Name the blood parasite species.
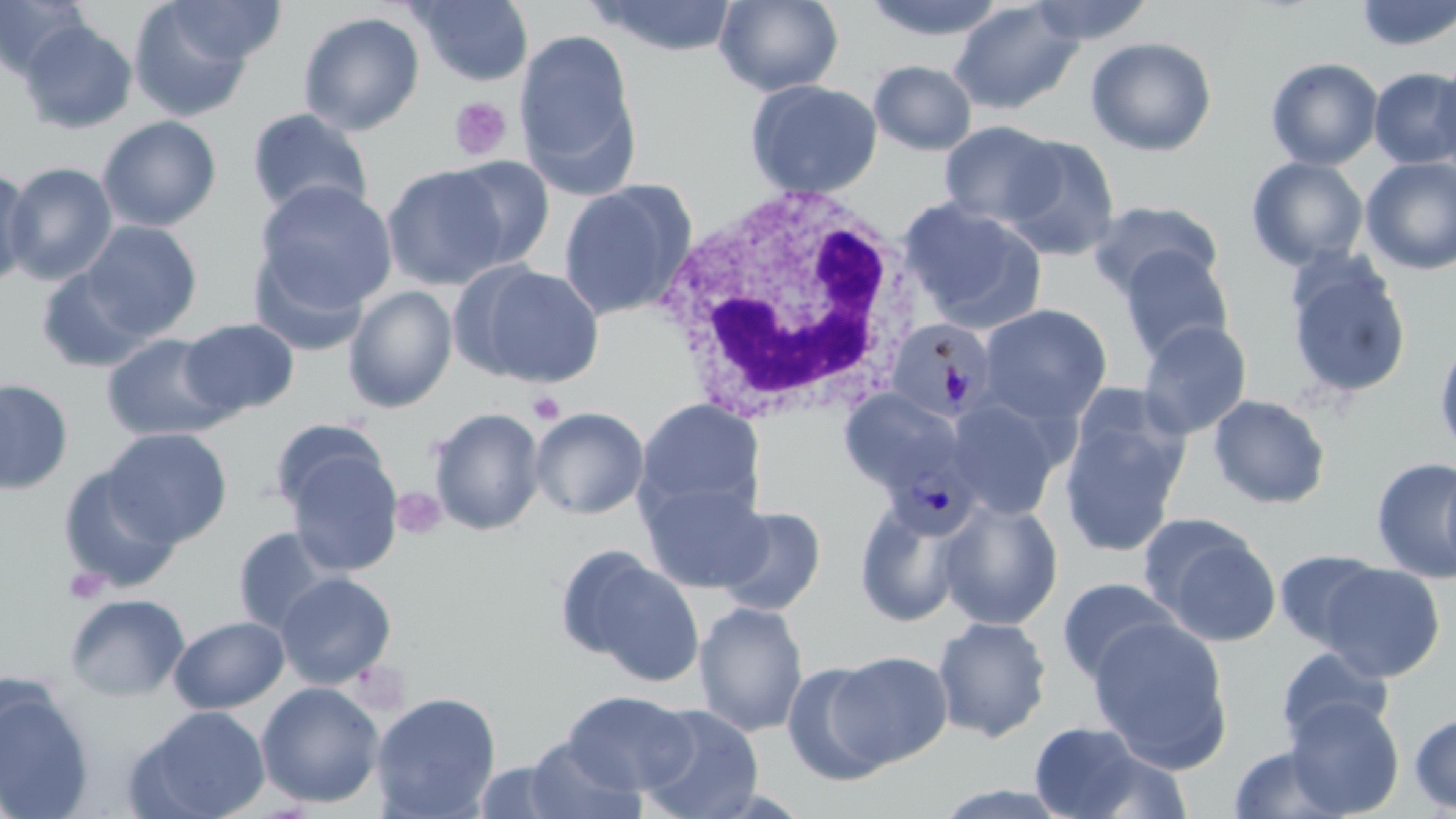

Plasmodium malariae.

image size = 1456×819 pixels
uninfected red blood cell locations = approximate bounding boxes as [x1, y1, x2, y2] in pixels: [0, 0, 94, 79], [409, 0, 534, 86], [588, 0, 740, 56], [713, 0, 844, 96], [859, 0, 1011, 42], [1025, 0, 1154, 45], [1354, 0, 1456, 51], [160, 1, 285, 66], [948, 1, 1084, 115], [129, 2, 256, 121], [298, 11, 425, 135], [19, 20, 137, 133], [514, 28, 640, 191], [1084, 36, 1217, 156], [1266, 57, 1384, 170], [1430, 58, 1456, 180], [868, 60, 977, 156], [1369, 67, 1456, 169], [745, 78, 883, 199], [246, 108, 373, 218], [97, 115, 222, 231], [939, 121, 1063, 226], [997, 134, 1121, 260], [441, 155, 556, 270], [1360, 156, 1456, 275], [1246, 157, 1369, 270], [2, 162, 118, 285], [381, 163, 511, 290], [0, 167, 36, 288], [558, 179, 697, 320], [253, 180, 398, 314], [899, 198, 1047, 332], [1087, 200, 1222, 303], [79, 221, 202, 338], [1117, 245, 1235, 363], [248, 248, 372, 357], [1285, 252, 1413, 402], [455, 260, 604, 389], [36, 265, 158, 373], [342, 285, 458, 413], [978, 304, 1113, 426], [178, 317, 300, 419], [1136, 320, 1252, 440], [101, 333, 233, 441], [1433, 333, 1456, 462], [0, 377, 74, 495], [837, 388, 968, 496], [1057, 394, 1191, 558], [1208, 394, 1331, 509], [635, 397, 766, 523], [945, 398, 1067, 520], [530, 406, 649, 520], [428, 407, 546, 536], [102, 428, 232, 546], [279, 441, 403, 578], [1371, 457, 1456, 583], [1441, 459, 1456, 585], [57, 463, 184, 593], [640, 477, 769, 593], [939, 498, 1064, 630], [854, 501, 967, 628], [713, 504, 827, 616], [1142, 516, 1282, 647], [232, 526, 344, 636], [557, 546, 703, 685], [1275, 550, 1386, 651], [1316, 563, 1446, 683], [274, 571, 397, 689], [1056, 577, 1181, 686], [65, 593, 190, 701], [694, 600, 809, 737], [169, 615, 289, 713], [932, 616, 1053, 742], [1087, 619, 1232, 770], [1275, 646, 1393, 747], [830, 650, 954, 766], [781, 662, 897, 786], [256, 681, 385, 808], [0, 683, 95, 819], [562, 690, 696, 796], [371, 691, 501, 818], [1283, 697, 1405, 817], [638, 704, 764, 819], [130, 705, 271, 819], [1409, 711, 1456, 814], [1029, 721, 1154, 818], [520, 737, 648, 819], [1226, 743, 1351, 819]
magnification = 1000x
stain = May-Grünwald-Giemsa
Plasmodium malariae-infected red blood cell locations = approximate bounding boxes as [x1, y1, x2, y2] in pixels: [891, 319, 995, 420], [884, 452, 978, 540]
preparation = thin blood smear
modality = optical microscopy
platelet locations = approximate bounding boxes as [x1, y1, x2, y2] in pixels: [448, 97, 512, 161], [527, 391, 565, 424], [392, 488, 448, 540], [64, 566, 109, 604]
white blood cell locations = approximate bounding boxes as [x1, y1, x2, y2] in pixels: [654, 181, 923, 429]
field of view = single